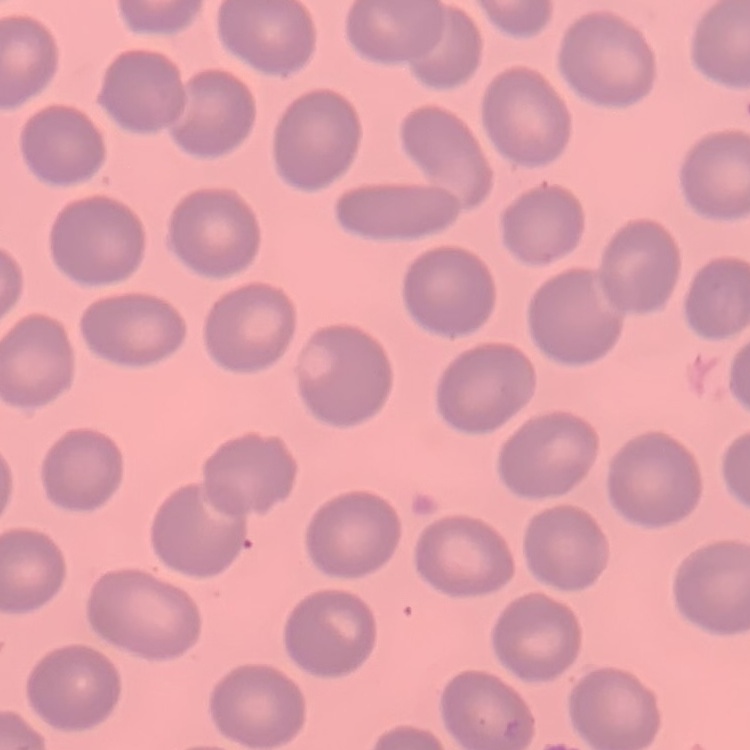 The red blood cells exhibit no rouleaux formation. Thin blood film. One tile cut from a larger photomicrograph. Stained with either Field's or Giemsa.